Describe the morphology of the erythrocytes.
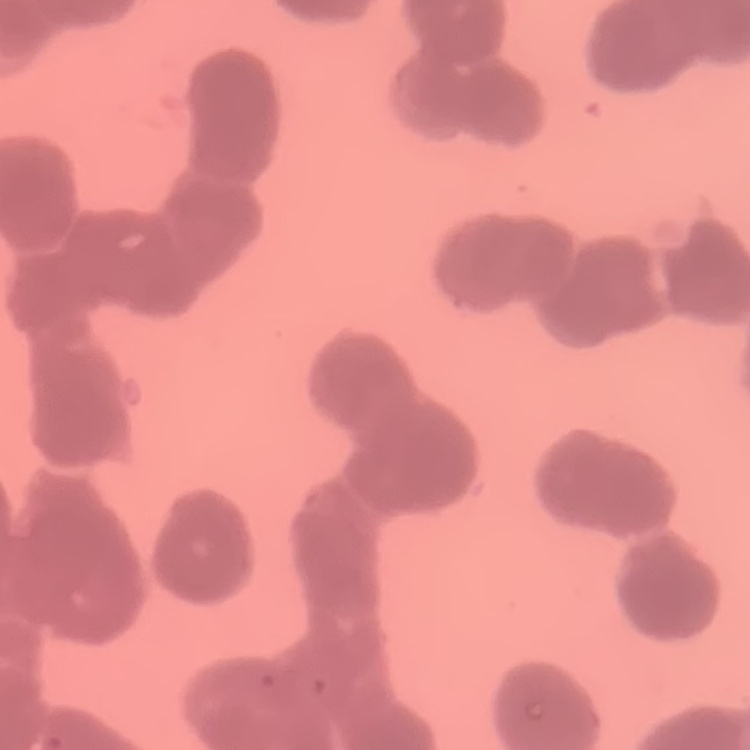
Rouleaux formation.

Summary:
  - Preparation: thin blood smear
  - Stain: Field's or Giemsa
  - Image type: square crop of a larger photomicrograph